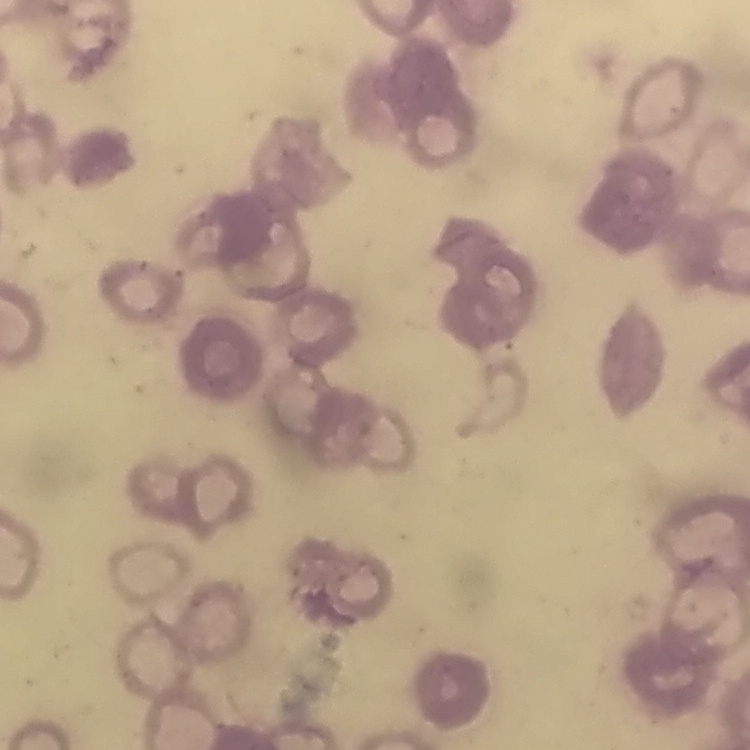
red blood cell morphology = rouleaux formation
preparation = thin blood film
stain = Field's or Giemsa
image type = one tile cut from a larger photomicrograph